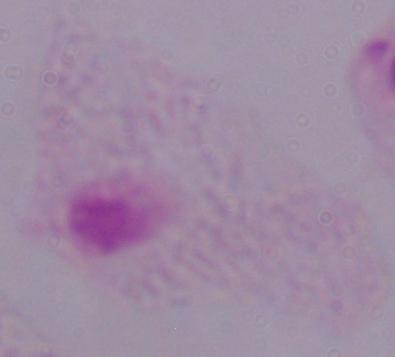 1000x magnification. Micrograph. A trichomonad is shown.